Classify this cell by malaria status.
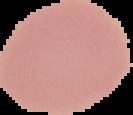

It is uninfected.

image size = 133×115 pixels
image type = cell region segmented out of the field of view; surrounding area masked to black
preparation = thin blood film